Report the malaria status of this cell.
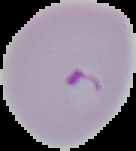
It is parasitized.

image size = 136×151 pixels
image type = segmented cell region with the area outside set to black
preparation = thin blood smear